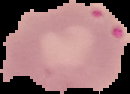 From a thin blood smear. Malaria status: uninfected. Image is 130×94 pixels. Segmented cell region on a black background.